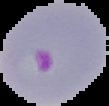

From a thin blood smear. Malaria status: parasitized. Image is 109×106 pixels. Segmented cell region on a black background.